Locate every Plasmodium parasite.
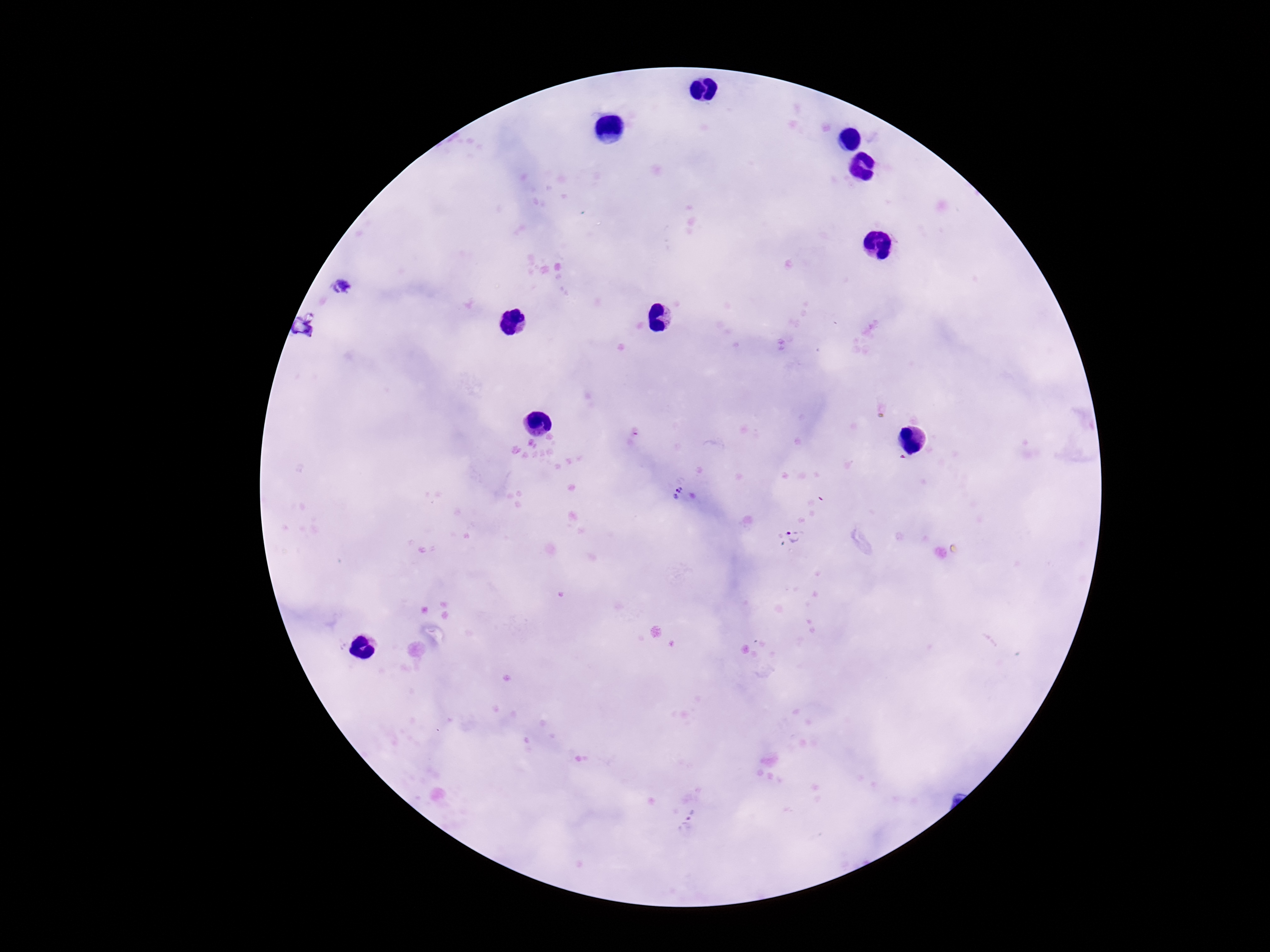

Approximate centers as {x, y} in pixels.
Plasmodium parasites: {344, 287}, {676, 491}, {795, 536}.

image size = 1270×952 pixels
magnification = 100x
stain = Giemsa
preparation = thick blood smear
capture = smartphone camera through the microscope eyepiece
field of view = single
patient malaria status = positive